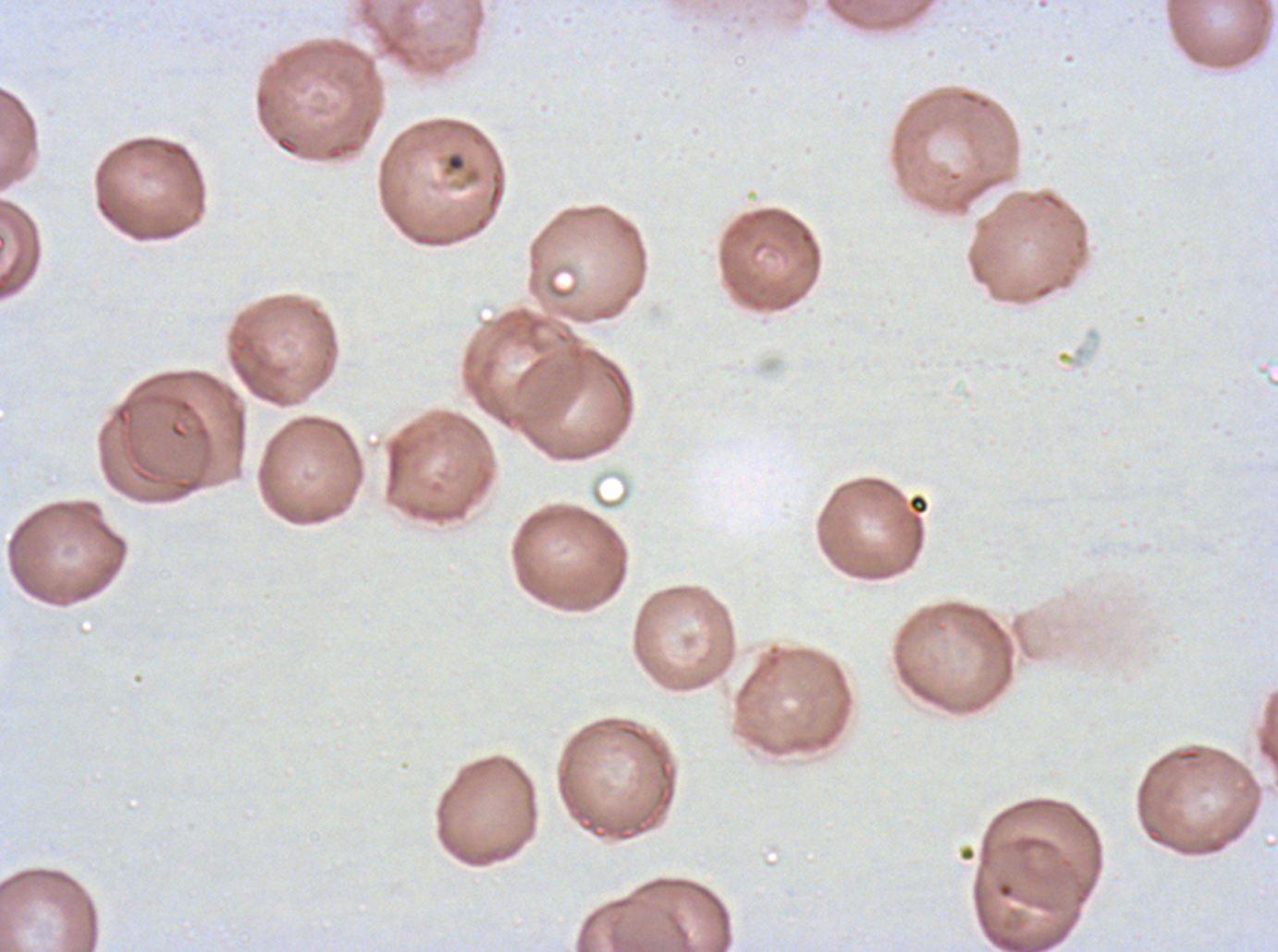
Approximate bounding rectangles given as corner coordinates in pixels from the top-left.
Summary:
  - Debris locations: (x1=445, y1=153, x2=466, y2=172), (x1=907, y1=494, x2=929, y2=515)
  - Field of view: sub-image separated from a larger composite
  - Image size: 1278×952 pixels
  - Preparation: thin blood film
  - Specimen: Plasmodium falciparum cultured ex vivo for 24 to 48 hours, from a patient in The Gambia
  - Stain: Giemsa